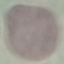

Summary:
  - Result: no malaria parasites seen
  - Capture: smartphone through the microscope eyepiece
  - Stain: Giemsa
  - Preparation: thin blood smear
  - Image type: cell patch, automatically extracted from a larger field of view and resized to 64 × 64 pixels